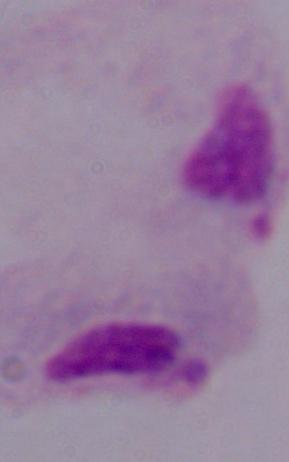
A trichomonad is shown. Captured at 1000x magnification. Micrograph.